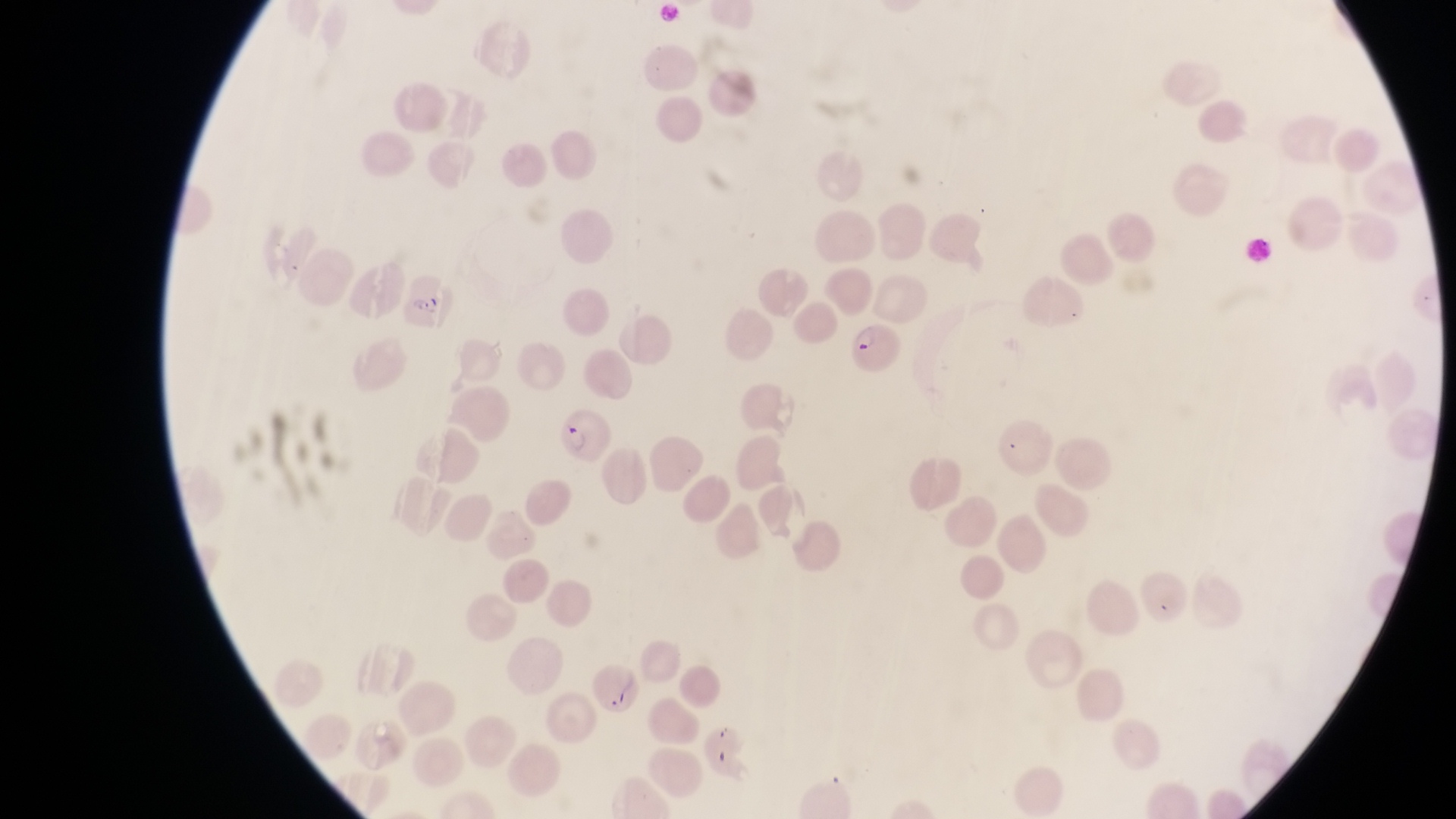

Approximate bounding boxes as [left, top, right, bottom] in pixels.
Summary:
  - Parasitised red blood cell locations: [404, 277, 459, 324], [849, 323, 905, 375], [554, 413, 617, 469]
  - Artifact (platelet-like body, stain precipitate, or debris) locations: [601, 682, 627, 705]
  - Magnification: 1000x
  - Field of view: single
  - Capture: smartphone photograph through the eyepiece of an Olympus CX-23 microscope
  - Image size: 1456×819 pixels
  - Preparation: thin blood smear
  - Country: Uganda